Give the extent of all Plasmodium falciparum-infected red blood cells.
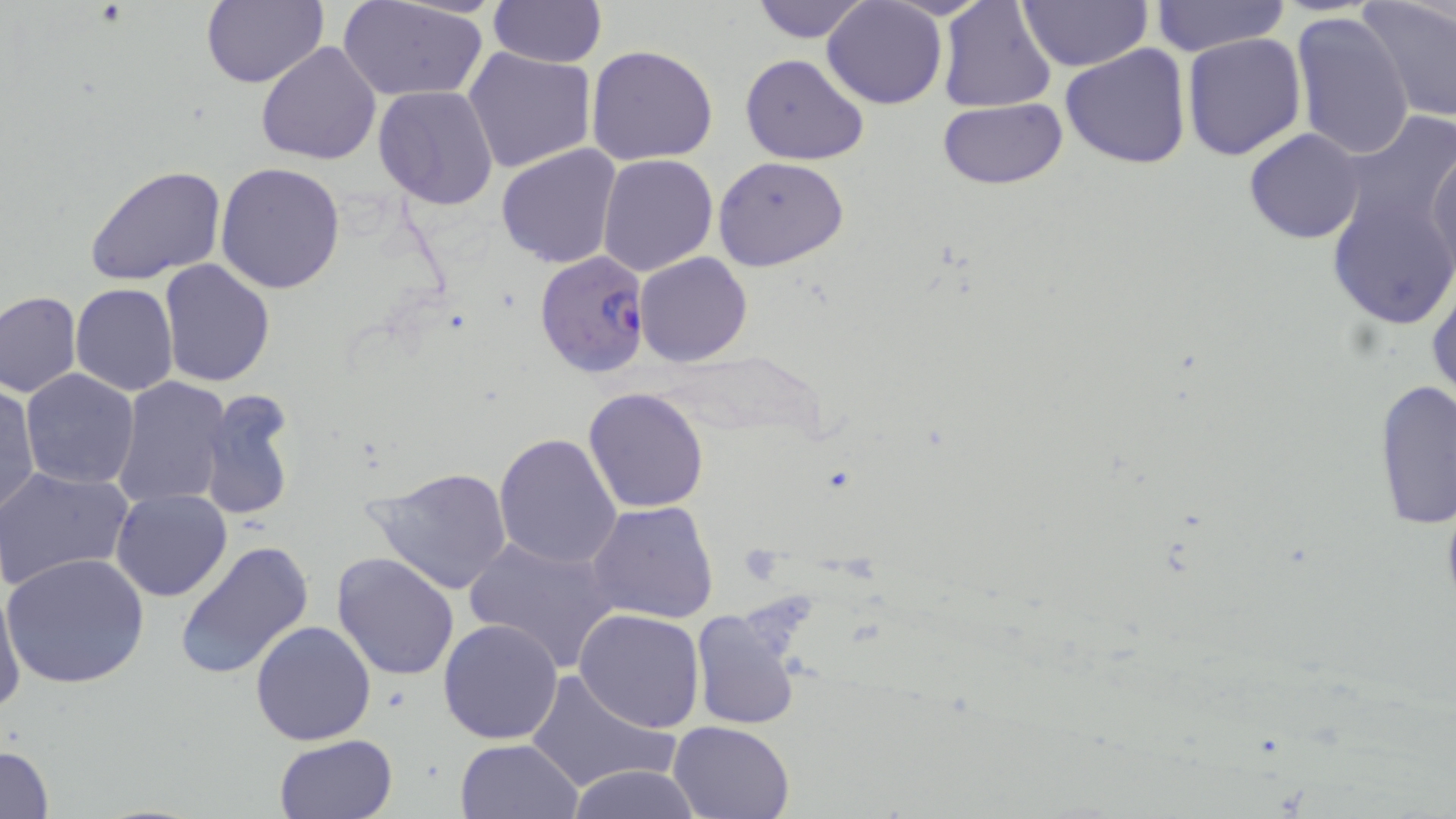
Approximate bounding boxes as named x1/y1/x2/y2 corners in pixels.
Plasmodium falciparum-infected red blood cells: (x1=534, y1=250, x2=650, y2=377).

slide-level diagnosis = Plasmodium falciparum
uninfected red blood cell locations = approximate bounding boxes as named x1/y1/x2/y2 corners in pixels: (x1=202, y1=0, x2=328, y2=89), (x1=487, y1=0, x2=605, y2=69), (x1=748, y1=0, x2=874, y2=43), (x1=937, y1=0, x2=1057, y2=112), (x1=1014, y1=0, x2=1153, y2=72), (x1=1150, y1=0, x2=1289, y2=57), (x1=1361, y1=0, x2=1456, y2=121), (x1=341, y1=1, x2=488, y2=101), (x1=822, y1=1, x2=946, y2=109), (x1=1292, y1=11, x2=1416, y2=162), (x1=1182, y1=32, x2=1307, y2=160), (x1=256, y1=42, x2=383, y2=166), (x1=1060, y1=43, x2=1192, y2=169), (x1=464, y1=45, x2=598, y2=174), (x1=586, y1=45, x2=719, y2=167), (x1=742, y1=53, x2=870, y2=166), (x1=372, y1=85, x2=500, y2=211), (x1=939, y1=99, x2=1068, y2=189), (x1=1332, y1=109, x2=1456, y2=239), (x1=1244, y1=127, x2=1365, y2=245), (x1=1427, y1=143, x2=1456, y2=278), (x1=496, y1=144, x2=622, y2=267), (x1=597, y1=153, x2=719, y2=277), (x1=714, y1=156, x2=848, y2=273), (x1=216, y1=163, x2=346, y2=294), (x1=85, y1=164, x2=229, y2=284), (x1=1326, y1=186, x2=1456, y2=328), (x1=637, y1=253, x2=753, y2=367), (x1=158, y1=259, x2=275, y2=388), (x1=1427, y1=271, x2=1456, y2=411), (x1=71, y1=283, x2=178, y2=395), (x1=0, y1=290, x2=81, y2=398), (x1=19, y1=369, x2=140, y2=491), (x1=113, y1=378, x2=229, y2=507), (x1=1374, y1=379, x2=1456, y2=530), (x1=0, y1=385, x2=39, y2=518), (x1=584, y1=387, x2=710, y2=514), (x1=199, y1=391, x2=296, y2=522), (x1=493, y1=432, x2=622, y2=570), (x1=365, y1=463, x2=516, y2=595), (x1=0, y1=466, x2=132, y2=590), (x1=112, y1=488, x2=232, y2=602), (x1=587, y1=501, x2=719, y2=625), (x1=464, y1=532, x2=620, y2=673), (x1=174, y1=539, x2=315, y2=681), (x1=331, y1=551, x2=460, y2=681), (x1=2, y1=552, x2=151, y2=690), (x1=0, y1=579, x2=24, y2=715), (x1=689, y1=605, x2=804, y2=730), (x1=574, y1=608, x2=706, y2=733), (x1=438, y1=618, x2=564, y2=743), (x1=250, y1=621, x2=376, y2=746), (x1=524, y1=668, x2=680, y2=797), (x1=668, y1=720, x2=796, y2=819), (x1=274, y1=734, x2=399, y2=819), (x1=455, y1=738, x2=583, y2=819), (x1=1, y1=744, x2=54, y2=818), (x1=565, y1=764, x2=704, y2=819)
magnification = 1000x
image size = 1456×819 pixels
field of view = single
modality = light microscopy
preparation = thin blood film
stain = May-Grünwald-Giemsa